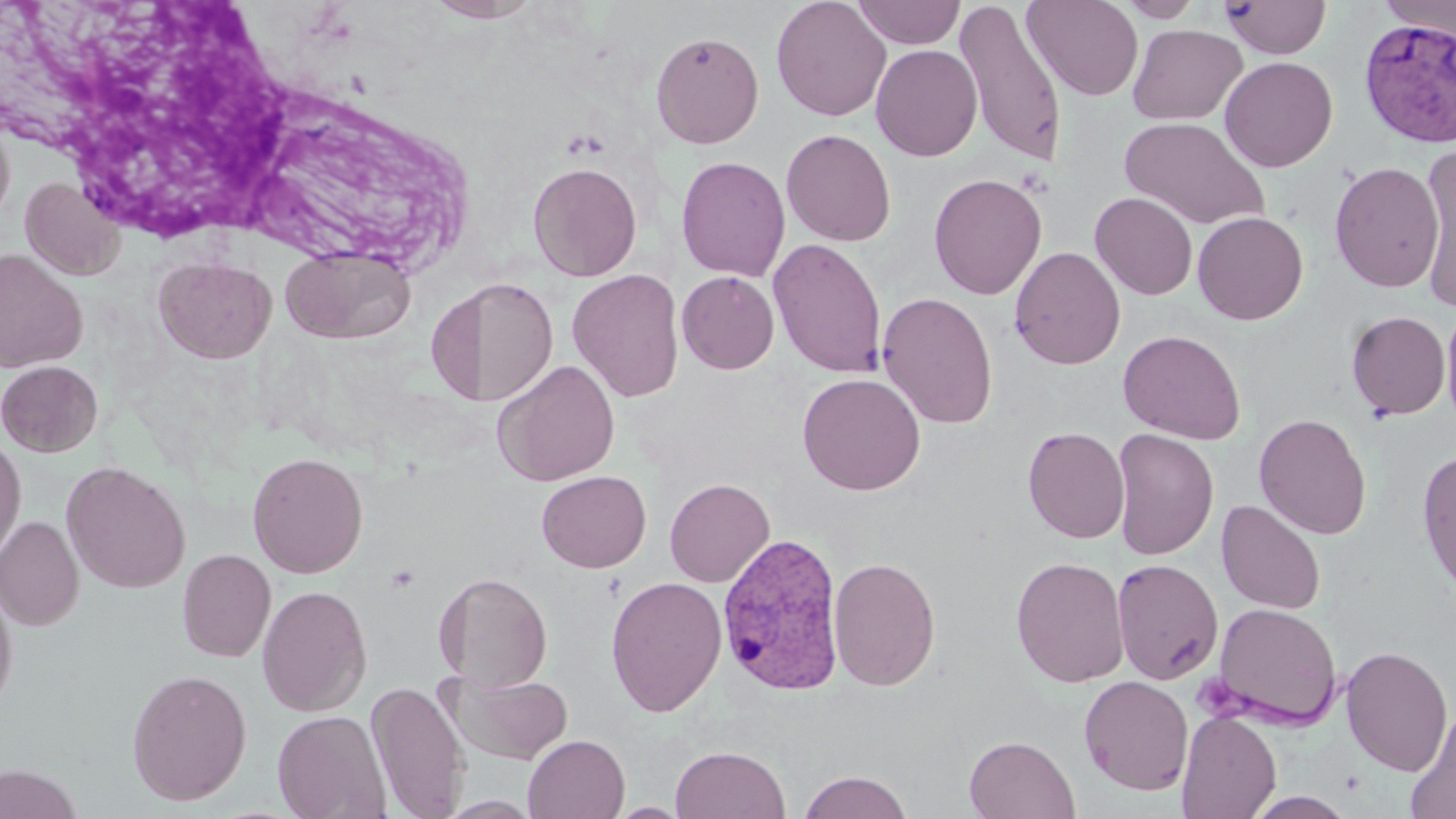

Summary:
  - Coordinate format: approximate bounding boxes as named x1/y1/x2/y2 corners in pixels
  - Uninfected red blood cell locations: (x1=424, y1=0, x2=541, y2=23), (x1=771, y1=0, x2=891, y2=121), (x1=851, y1=0, x2=965, y2=48), (x1=1022, y1=0, x2=1143, y2=101), (x1=1116, y1=0, x2=1204, y2=22), (x1=1220, y1=0, x2=1332, y2=59), (x1=1378, y1=0, x2=1456, y2=40), (x1=954, y1=2, x2=1067, y2=168), (x1=1128, y1=23, x2=1247, y2=125), (x1=651, y1=30, x2=764, y2=148), (x1=870, y1=44, x2=983, y2=161), (x1=1219, y1=55, x2=1338, y2=172), (x1=0, y1=112, x2=15, y2=229), (x1=1120, y1=115, x2=1269, y2=230), (x1=781, y1=128, x2=897, y2=246), (x1=1416, y1=151, x2=1455, y2=306), (x1=676, y1=155, x2=791, y2=282), (x1=527, y1=161, x2=643, y2=281), (x1=1329, y1=161, x2=1444, y2=293), (x1=929, y1=172, x2=1047, y2=299), (x1=21, y1=177, x2=126, y2=280), (x1=1090, y1=192, x2=1198, y2=300), (x1=1192, y1=211, x2=1308, y2=325), (x1=768, y1=238, x2=887, y2=378), (x1=280, y1=246, x2=416, y2=345), (x1=1009, y1=246, x2=1125, y2=370), (x1=0, y1=249, x2=88, y2=373), (x1=153, y1=256, x2=277, y2=364), (x1=567, y1=268, x2=685, y2=402), (x1=677, y1=271, x2=779, y2=374), (x1=441, y1=275, x2=559, y2=408), (x1=877, y1=291, x2=999, y2=428), (x1=1440, y1=305, x2=1456, y2=433), (x1=1346, y1=310, x2=1451, y2=420), (x1=1118, y1=329, x2=1246, y2=444), (x1=493, y1=359, x2=621, y2=486), (x1=0, y1=360, x2=103, y2=457), (x1=797, y1=372, x2=926, y2=495), (x1=1254, y1=412, x2=1372, y2=540), (x1=1023, y1=426, x2=1130, y2=543), (x1=1111, y1=428, x2=1219, y2=561), (x1=0, y1=435, x2=26, y2=563), (x1=1417, y1=447, x2=1456, y2=597), (x1=247, y1=451, x2=369, y2=579), (x1=61, y1=460, x2=192, y2=594), (x1=537, y1=470, x2=651, y2=572), (x1=664, y1=477, x2=775, y2=587), (x1=1216, y1=499, x2=1326, y2=615), (x1=0, y1=515, x2=84, y2=630), (x1=177, y1=549, x2=276, y2=663), (x1=1010, y1=556, x2=1130, y2=687), (x1=828, y1=557, x2=941, y2=690), (x1=1112, y1=558, x2=1224, y2=685), (x1=440, y1=570, x2=553, y2=693), (x1=606, y1=576, x2=727, y2=716), (x1=0, y1=578, x2=18, y2=716), (x1=433, y1=578, x2=466, y2=682), (x1=257, y1=584, x2=372, y2=717), (x1=1210, y1=602, x2=1343, y2=730), (x1=1340, y1=645, x2=1453, y2=776), (x1=126, y1=668, x2=252, y2=806), (x1=453, y1=673, x2=573, y2=764), (x1=1079, y1=675, x2=1194, y2=795), (x1=367, y1=680, x2=468, y2=818), (x1=1403, y1=708, x2=1456, y2=819), (x1=272, y1=709, x2=392, y2=819), (x1=1176, y1=709, x2=1281, y2=819), (x1=523, y1=734, x2=630, y2=818), (x1=964, y1=734, x2=1080, y2=819), (x1=670, y1=745, x2=791, y2=819), (x1=0, y1=763, x2=86, y2=819), (x1=799, y1=770, x2=912, y2=819), (x1=1245, y1=792, x2=1357, y2=818), (x1=437, y1=796, x2=541, y2=818), (x1=608, y1=802, x2=691, y2=817)
  - Plasmodium vivax-infected red blood cell locations: (x1=1359, y1=17, x2=1456, y2=148), (x1=717, y1=531, x2=846, y2=696)
  - Platelet locations: (x1=384, y1=563, x2=421, y2=593)
  - Slide-level diagnosis: Plasmodium vivax
  - Field of view: one of a larger specimen
  - Preparation: thin blood smear
  - Image size: 1456×819 pixels
  - Magnification: 1000x
  - Modality: light microscopy
  - Stain: May-Grünwald-Giemsa